Describe the morphology of the red blood cells.
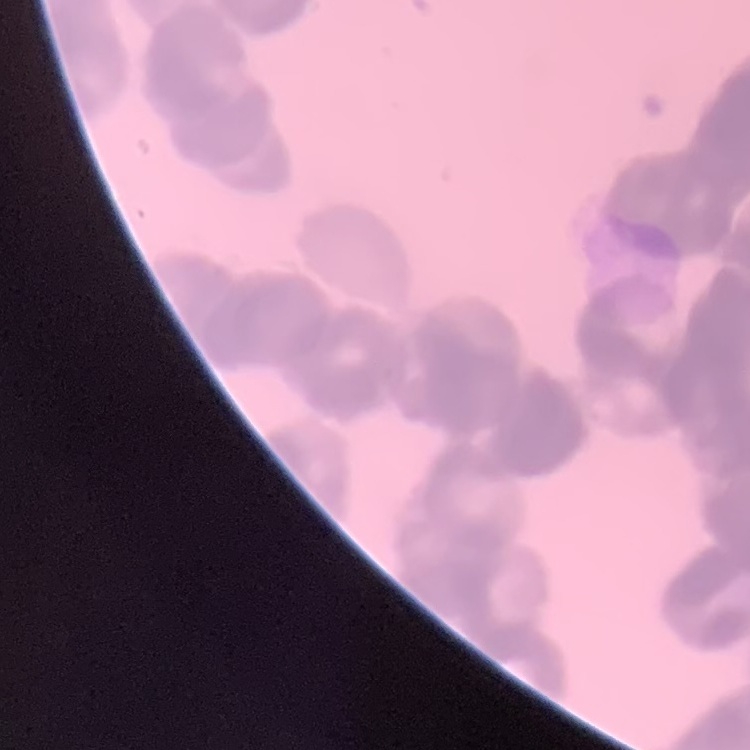
Rouleaux formation.

stain = Field's or Giemsa
preparation = thin blood film
image type = square crop of a larger photomicrograph